Locate every Plasmodium vivax-infected red blood cell.
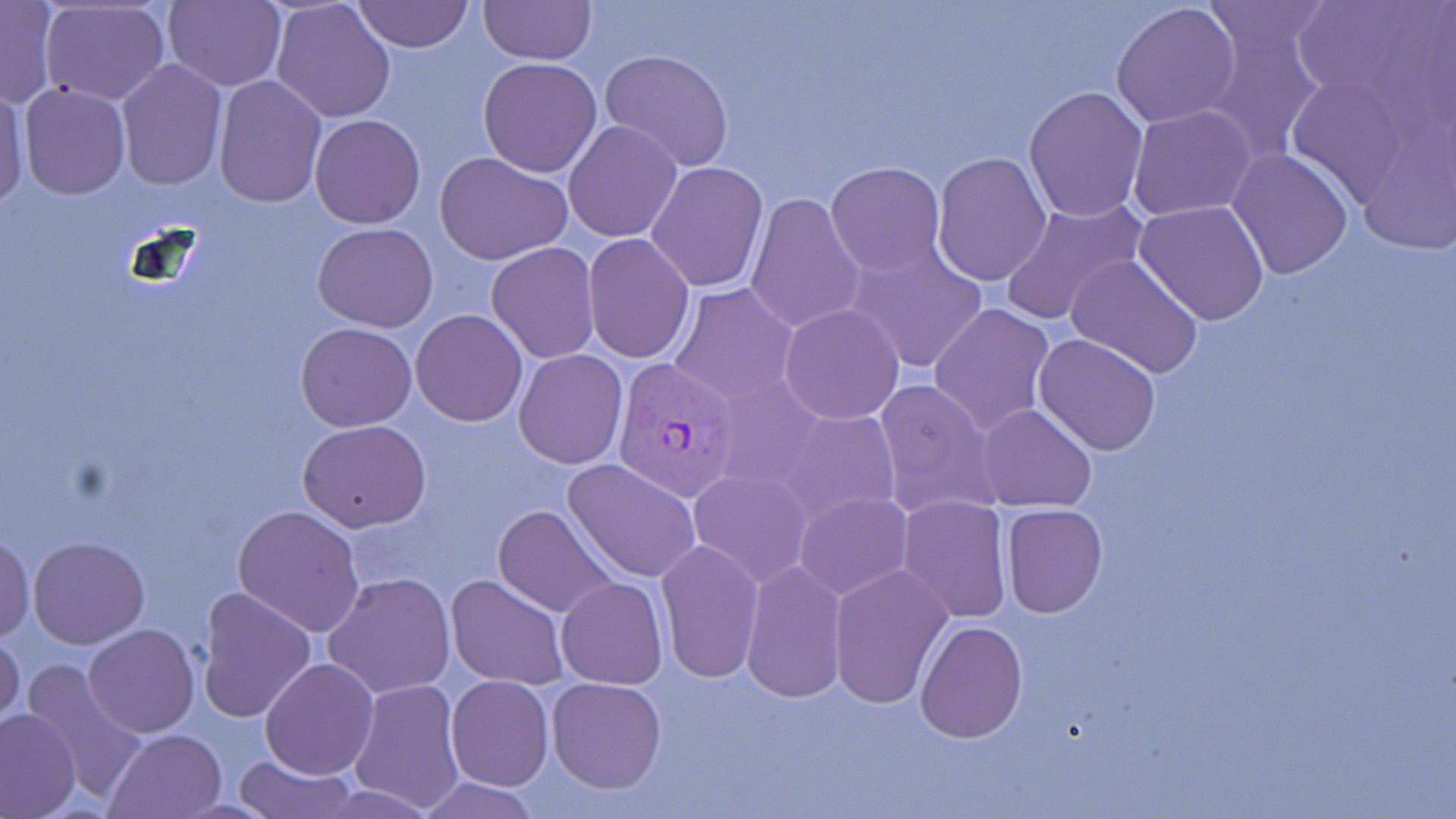

Approximate bounding boxes as named x1/y1/x2/y2 corners in pixels.
Plasmodium vivax-infected red blood cells: (x1=612, y1=359, x2=742, y2=500).

Summary:
  - Uninfected red blood cell locations: (x1=162, y1=0, x2=285, y2=90), (x1=352, y1=0, x2=472, y2=53), (x1=478, y1=0, x2=596, y2=66), (x1=1288, y1=0, x2=1452, y2=129), (x1=1, y1=1, x2=61, y2=109), (x1=38, y1=2, x2=169, y2=105), (x1=271, y1=2, x2=396, y2=121), (x1=1111, y1=3, x2=1242, y2=130), (x1=1198, y1=3, x2=1336, y2=57), (x1=1202, y1=21, x2=1327, y2=161), (x1=598, y1=49, x2=735, y2=172), (x1=477, y1=57, x2=602, y2=177), (x1=116, y1=60, x2=226, y2=192), (x1=212, y1=76, x2=326, y2=209), (x1=0, y1=82, x2=29, y2=208), (x1=20, y1=83, x2=130, y2=200), (x1=1024, y1=84, x2=1148, y2=221), (x1=1129, y1=105, x2=1259, y2=222), (x1=309, y1=114, x2=425, y2=229), (x1=563, y1=119, x2=683, y2=243), (x1=1226, y1=148, x2=1353, y2=281), (x1=434, y1=150, x2=573, y2=266), (x1=930, y1=151, x2=1052, y2=286), (x1=827, y1=161, x2=945, y2=274), (x1=645, y1=162, x2=769, y2=293), (x1=746, y1=192, x2=868, y2=335), (x1=999, y1=196, x2=1148, y2=325), (x1=1134, y1=199, x2=1269, y2=326), (x1=312, y1=223, x2=438, y2=330), (x1=583, y1=234, x2=695, y2=363), (x1=842, y1=241, x2=988, y2=374), (x1=485, y1=243, x2=600, y2=363), (x1=1066, y1=253, x2=1205, y2=378), (x1=667, y1=282, x2=802, y2=407), (x1=928, y1=302, x2=1056, y2=436), (x1=777, y1=303, x2=905, y2=425), (x1=411, y1=309, x2=527, y2=426), (x1=297, y1=323, x2=417, y2=432), (x1=1034, y1=334, x2=1162, y2=457), (x1=514, y1=349, x2=628, y2=471), (x1=872, y1=378, x2=1002, y2=520), (x1=975, y1=403, x2=1097, y2=513), (x1=777, y1=409, x2=901, y2=528), (x1=298, y1=420, x2=431, y2=532), (x1=564, y1=458, x2=701, y2=582), (x1=687, y1=468, x2=813, y2=586), (x1=793, y1=492, x2=912, y2=601), (x1=898, y1=494, x2=1011, y2=622), (x1=232, y1=503, x2=366, y2=636), (x1=1000, y1=503, x2=1108, y2=618), (x1=493, y1=504, x2=619, y2=617), (x1=0, y1=528, x2=34, y2=643), (x1=28, y1=536, x2=149, y2=648), (x1=656, y1=540, x2=764, y2=684), (x1=740, y1=561, x2=847, y2=703), (x1=829, y1=564, x2=953, y2=709), (x1=323, y1=573, x2=454, y2=699), (x1=445, y1=574, x2=568, y2=690), (x1=556, y1=576, x2=669, y2=689), (x1=196, y1=586, x2=317, y2=725), (x1=916, y1=620, x2=1027, y2=741), (x1=83, y1=624, x2=200, y2=736), (x1=0, y1=631, x2=24, y2=735), (x1=261, y1=658, x2=378, y2=780), (x1=21, y1=660, x2=148, y2=804), (x1=446, y1=676, x2=553, y2=791), (x1=547, y1=677, x2=666, y2=793), (x1=348, y1=678, x2=466, y2=813), (x1=0, y1=708, x2=81, y2=817), (x1=104, y1=728, x2=226, y2=818), (x1=234, y1=753, x2=360, y2=819), (x1=410, y1=777, x2=546, y2=817)
  - Slide-level diagnosis: Plasmodium vivax
  - Modality: light microscopy
  - Magnification: 1000x
  - Stain: May-Grünwald-Giemsa
  - Image size: 1456×819 pixels
  - Preparation: thin blood smear
  - Field of view: one of a larger specimen